Report the malaria status of this cell.
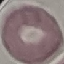
It is uninfected.

Thin smear of blood. Automatically extracted cell patch, resized to 64 × 64 pixels. Photographed with a smartphone camera at the microscope eyepiece. Giemsa stain.